State which parasite is depicted.
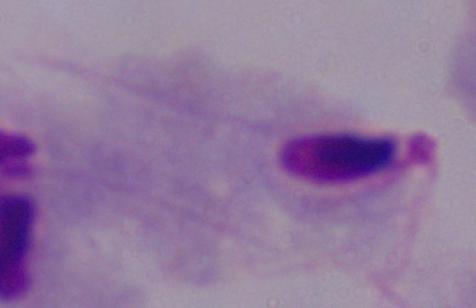

A trichomonad.

Summary:
  - Modality: photomicrograph
  - Magnification: 1000x